Evaluate for Plasmodium parasites.
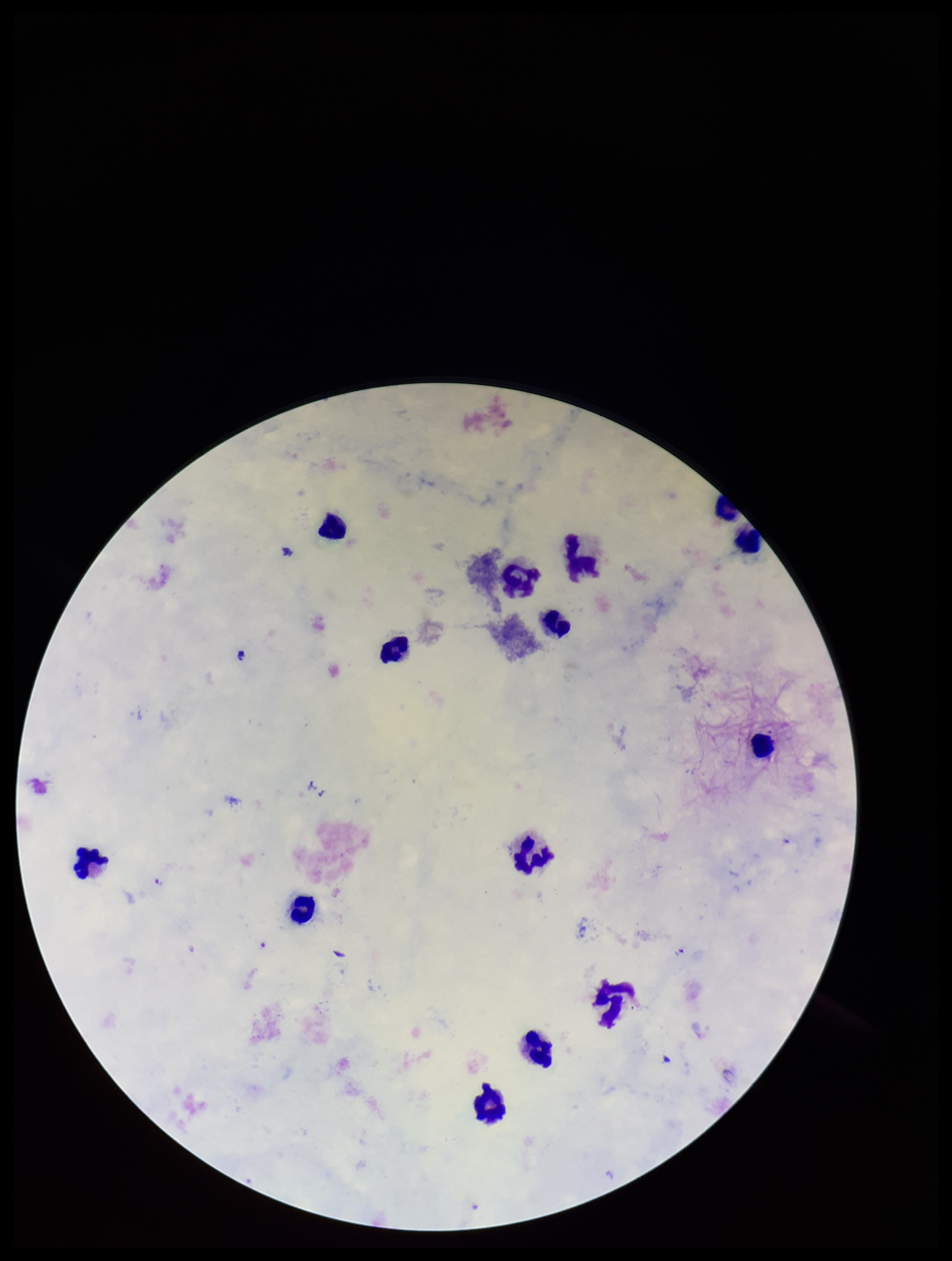

Seen.

Preparation: thick smear. Giemsa stain. Patient malaria status: infected. Parasite count: 1. Species reported for this patient: Plasmodium falciparum. Single field of view. Photographed through the microscope eyepiece with a smartphone camera. Image is 952×1261 pixels. Leukocyte count: 14.